Locate every malaria parasite.
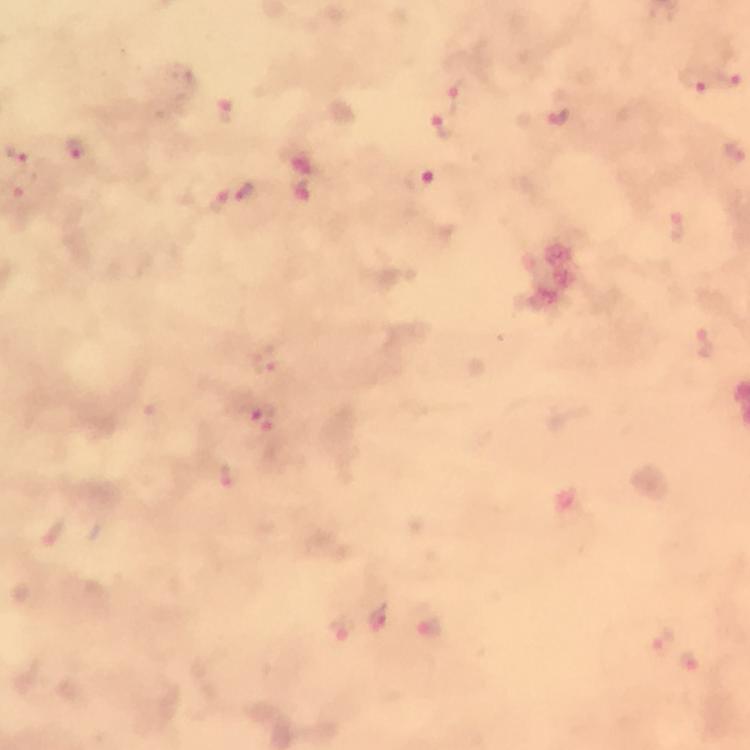
Approximate centers as (x, y) in pixels.
Malaria parasites: (729, 74), (692, 82), (459, 95), (226, 112), (557, 117), (444, 124), (18, 150), (732, 151), (76, 153), (419, 179), (23, 182), (246, 193), (302, 194), (222, 199), (705, 343), (267, 361), (261, 418), (231, 476), (378, 621), (340, 629), (430, 629), (662, 639), (690, 666).

100x magnification. Thick blood film. Giemsa stain. Immersion oil applied. Image is 750×750 pixels. From a diagnostic examination for malaria. A crop from one field of view. Smartphone photograph taken through a microscope.